Describe the morphology of the erythrocytes.
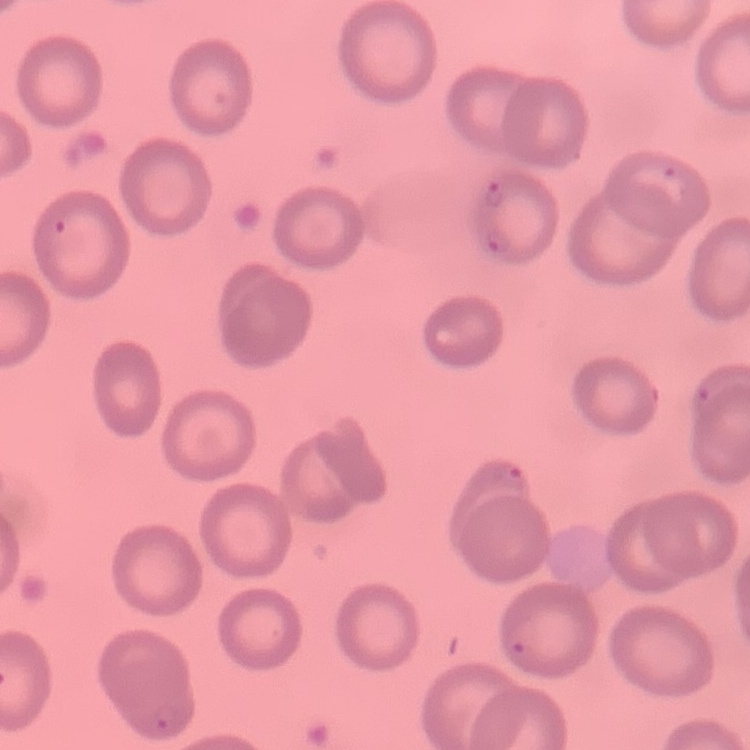
No rouleaux formation.

Thin blood film. Field's or Giemsa stain. Square crop of a larger photomicrograph.